Assess this cell for malaria.
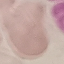

Uninfected.

Thin blood smear. Automatically extracted cell patch, resized to 64 × 64 pixels. Giemsa-stained preparation. Photographed with a smartphone camera at the microscope eyepiece.